Assess the background quality.
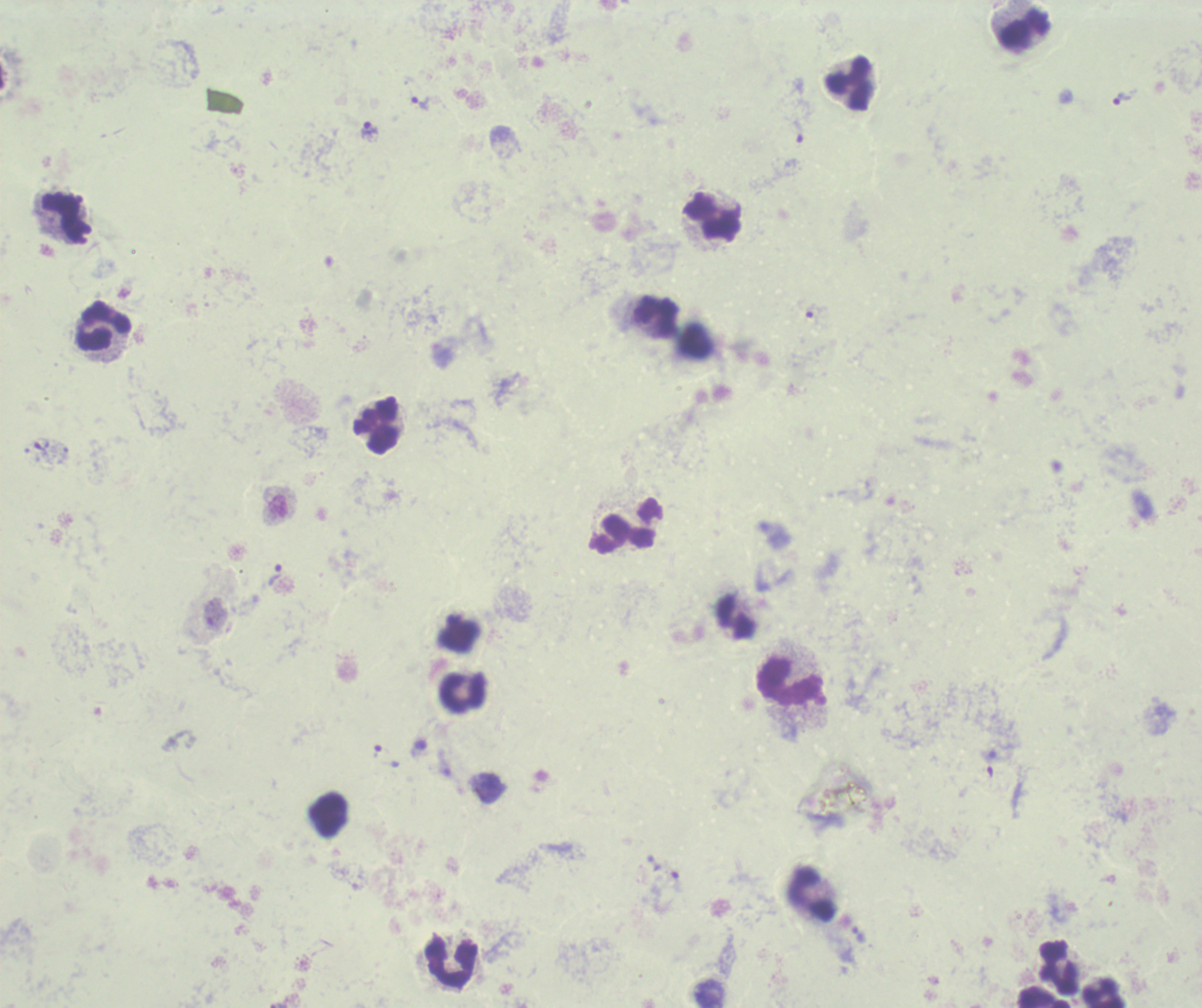
It is poor.

coordinate format = approximate centers as [x, y] in pixels
trophozoite locations = [1121, 99], [420, 104], [369, 132], [798, 132], [41, 447], [275, 575], [991, 763]
leukocyte locations = [1025, 30], [848, 83], [64, 216], [713, 217], [657, 315], [102, 326], [378, 426], [626, 524], [737, 618], [789, 680], [463, 692], [330, 813], [811, 893], [452, 962], [1060, 968], [1104, 992], [1043, 997]
magnification = 100x
result = malaria parasites detected
stain = Romanowsky
preparation = thick blood film
context = previously used in an actual diagnosis
image size = 1202×1008 pixels
field of view = one from this slide